Give the position of every malaria parasite.
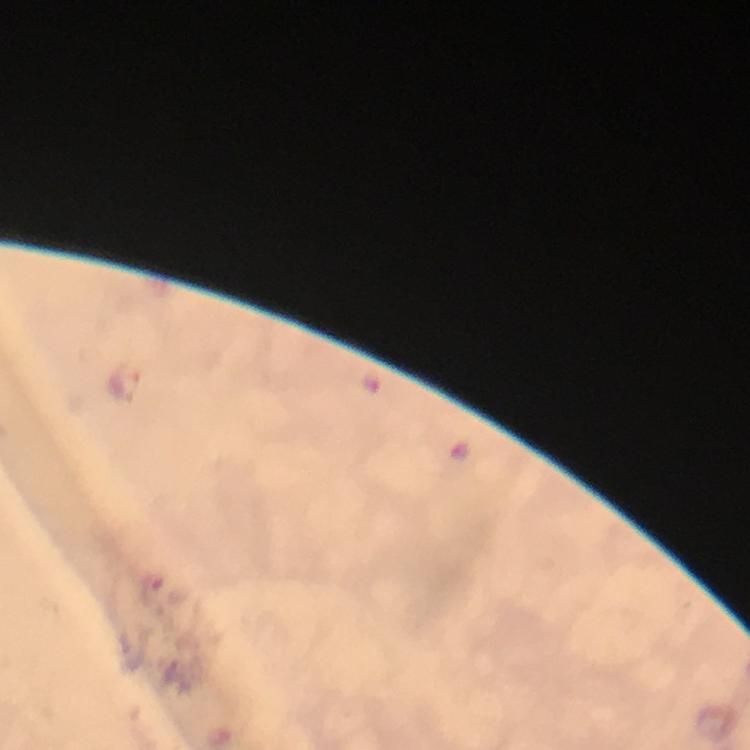
Approximate object centers, in pixels from the top-left corner.
Malaria parasites: (x=150, y=590).

Summary:
  - Immersion oil: applied
  - Preparation: thick blood smear
  - Image size: 750×750 pixels
  - Context: from a diagnostic examination for malaria
  - Cropped from: one field of view
  - Capture: smartphone mounted on the microscope
  - Stain: Giemsa
  - Magnification: 100x